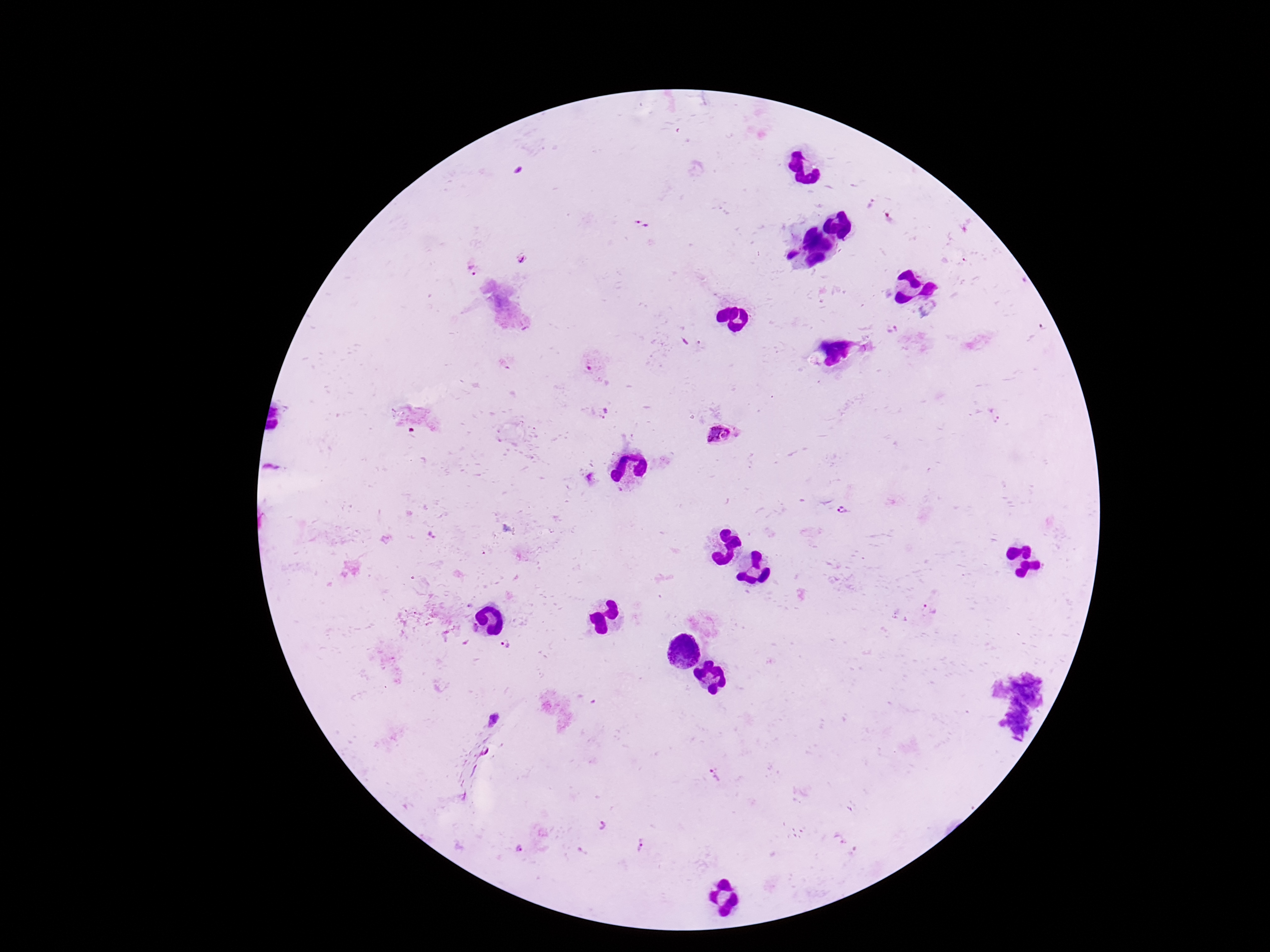

{
  "stain": "Giemsa",
  "capture": "smartphone camera through the microscope eyepiece",
  "magnification": "100x",
  "patient_malaria_status": "positive",
  "preparation": "thick peripheral-blood smear",
  "plasmodium_parasite_locations": "approximate centers as {x, y} in pixels: {643, 224}, {523, 258}, {473, 268}, {892, 329}, {605, 413}, {722, 434}, {844, 511}, {508, 644}, {493, 720}, {602, 825}, {642, 847}",
  "field_of_view": "single",
  "image_size": "1270×952 pixels"
}